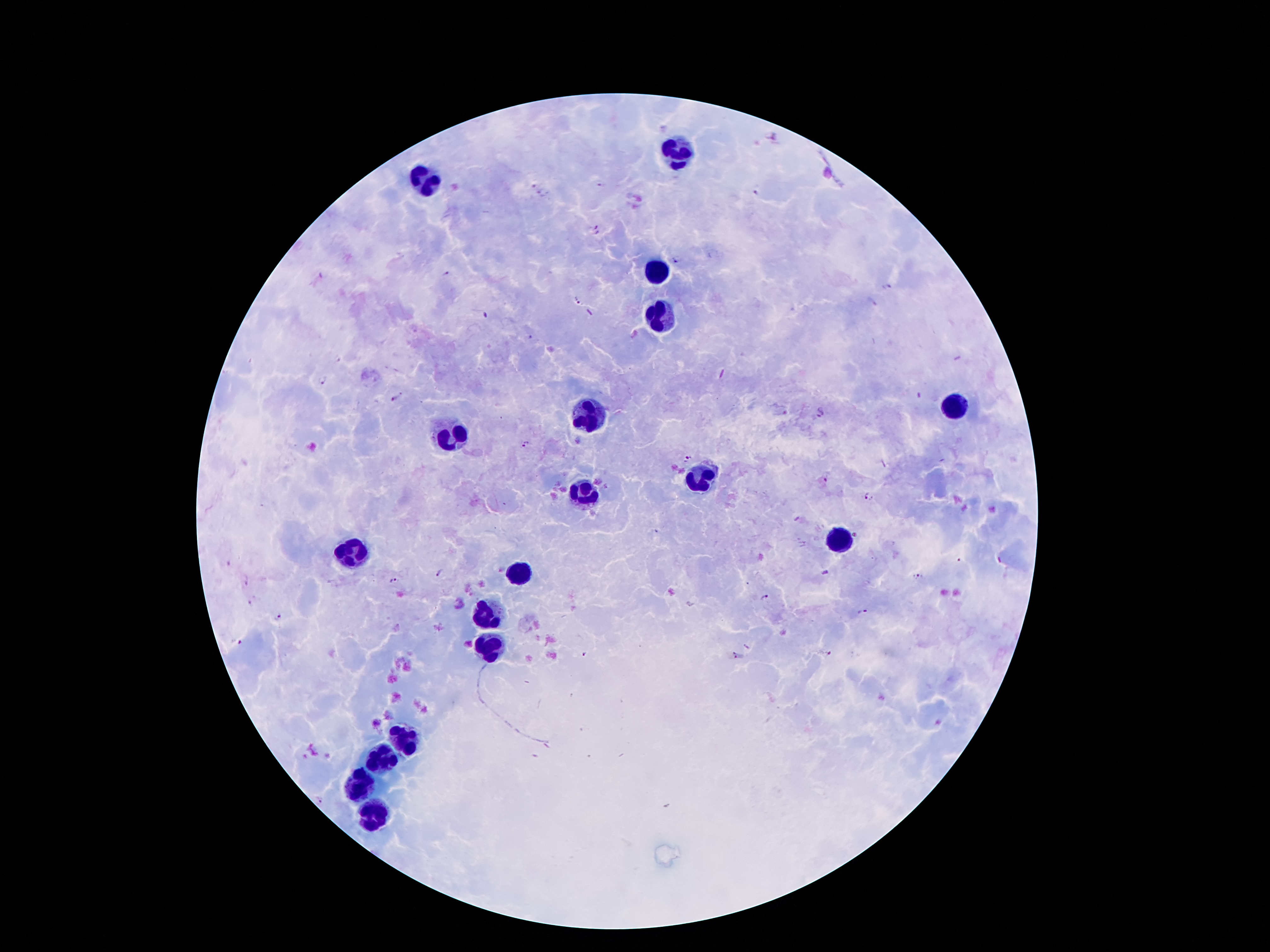
Approximate centers as (x, y) in pixels.
Summary:
  - Plasmodium parasite locations: (772, 138), (534, 185), (600, 186), (544, 193), (757, 193), (598, 230), (677, 260), (447, 274), (887, 285), (576, 301), (870, 304), (530, 338), (323, 381), (396, 398), (820, 413), (526, 444), (687, 459), (870, 497), (439, 574), (918, 576), (392, 581), (248, 583), (765, 598), (251, 603), (862, 612), (278, 617), (239, 642), (830, 652), (584, 655), (734, 655), (321, 800)
  - Leukocyte locations: (679, 155), (427, 177), (655, 272), (665, 317), (956, 407), (592, 414), (450, 436), (697, 479), (583, 492), (840, 539), (355, 552), (518, 576), (487, 612), (492, 646), (404, 744), (382, 757), (359, 787), (375, 817)
  - Magnification: 100x
  - Field of view: one from this slide
  - Stain: Giemsa
  - Image size: 1270×952 pixels
  - Preparation: thick blood smear
  - Patient malaria status: positive for Plasmodium falciparum
  - Capture: smartphone through the microscope eyepiece